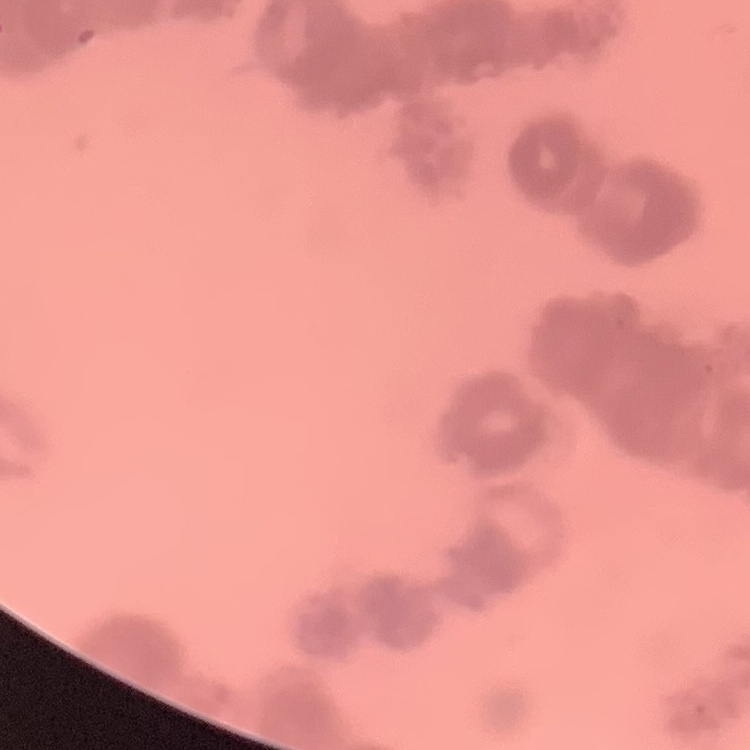

Summary:
  - Red blood cell morphology: rouleaux formation
  - Stain: Field's or Giemsa
  - Preparation: thin blood film
  - Image type: square crop of a larger photomicrograph